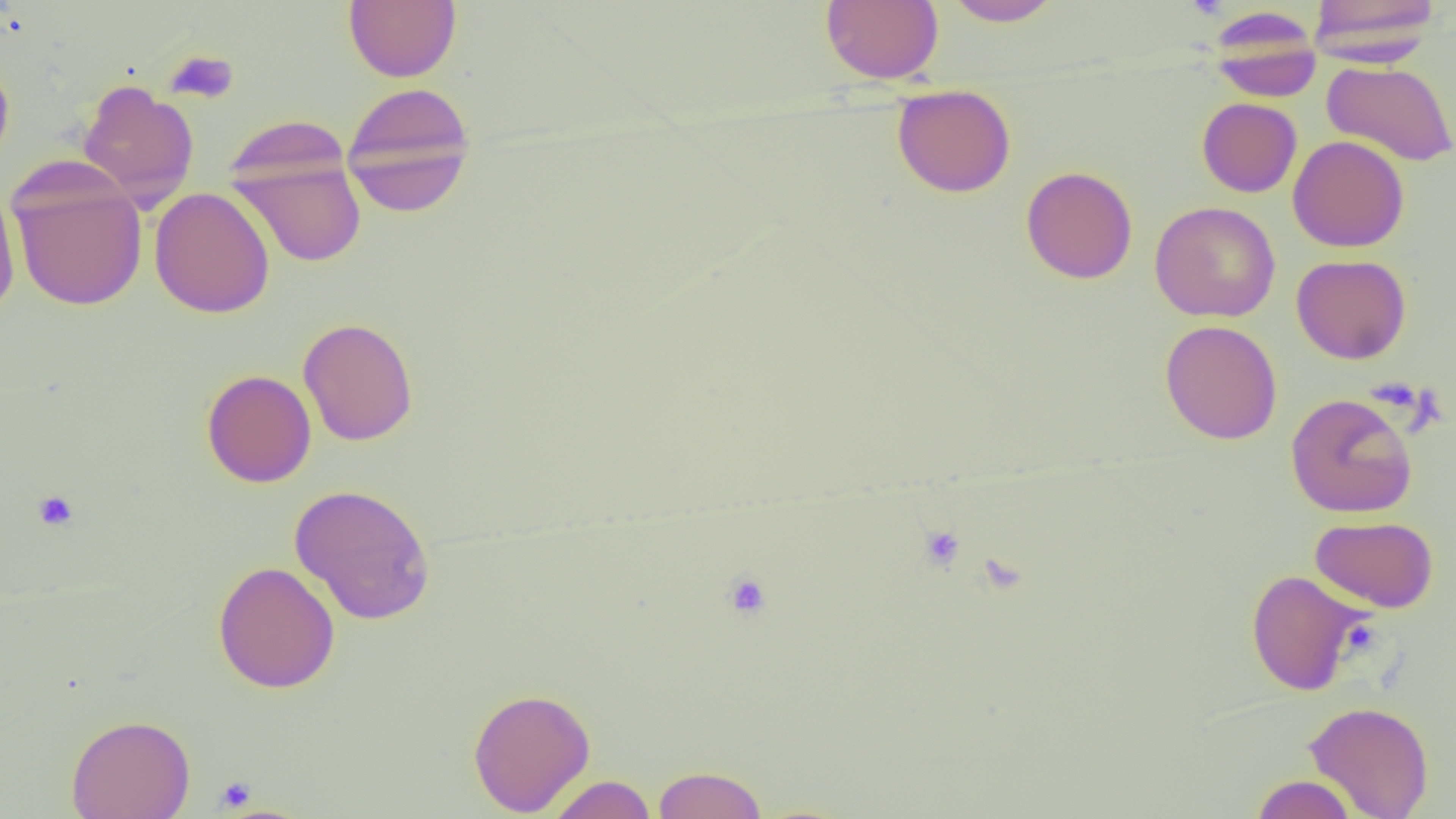

Approximate bounding boxes as named x1/y1/x2/y2 corners in pixels. Uninfected red blood cell locations: (x1=344, y1=0, x2=461, y2=83), (x1=821, y1=0, x2=943, y2=84), (x1=942, y1=0, x2=1064, y2=27), (x1=1307, y1=0, x2=1440, y2=62), (x1=1207, y1=8, x2=1322, y2=102), (x1=0, y1=53, x2=15, y2=171), (x1=1322, y1=61, x2=1456, y2=166), (x1=78, y1=79, x2=199, y2=208), (x1=340, y1=83, x2=476, y2=216), (x1=892, y1=84, x2=1016, y2=198), (x1=1197, y1=97, x2=1302, y2=197), (x1=222, y1=114, x2=352, y2=193), (x1=1288, y1=135, x2=1410, y2=252), (x1=229, y1=152, x2=367, y2=268), (x1=1021, y1=166, x2=1138, y2=284), (x1=8, y1=168, x2=148, y2=312), (x1=0, y1=184, x2=20, y2=316), (x1=149, y1=187, x2=275, y2=318), (x1=1150, y1=201, x2=1281, y2=323), (x1=1291, y1=254, x2=1412, y2=364), (x1=298, y1=317, x2=418, y2=446), (x1=1160, y1=319, x2=1283, y2=445), (x1=201, y1=370, x2=316, y2=487), (x1=1285, y1=393, x2=1417, y2=518), (x1=289, y1=484, x2=436, y2=625), (x1=1310, y1=516, x2=1438, y2=612), (x1=213, y1=560, x2=340, y2=694), (x1=1245, y1=569, x2=1368, y2=695), (x1=467, y1=687, x2=595, y2=816), (x1=1304, y1=701, x2=1434, y2=819), (x1=66, y1=713, x2=195, y2=819), (x1=652, y1=765, x2=768, y2=818), (x1=1249, y1=774, x2=1359, y2=818), (x1=546, y1=775, x2=657, y2=818). Platelet locations: (x1=1184, y1=0, x2=1230, y2=20), (x1=164, y1=49, x2=239, y2=104), (x1=32, y1=489, x2=79, y2=531), (x1=919, y1=525, x2=965, y2=571), (x1=723, y1=572, x2=772, y2=619), (x1=214, y1=776, x2=256, y2=812). Slide-level diagnosis: negative for blood parasites. Thin blood film. Captured at 1000x magnification. Light microscopy. Image is 1456×819 pixels. Single field of view.